Report the malaria status of this cell.
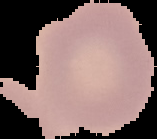

Uninfected.

From a thin blood film. Image is 157×139 pixels. The area outside the segmented cell region is set to black.